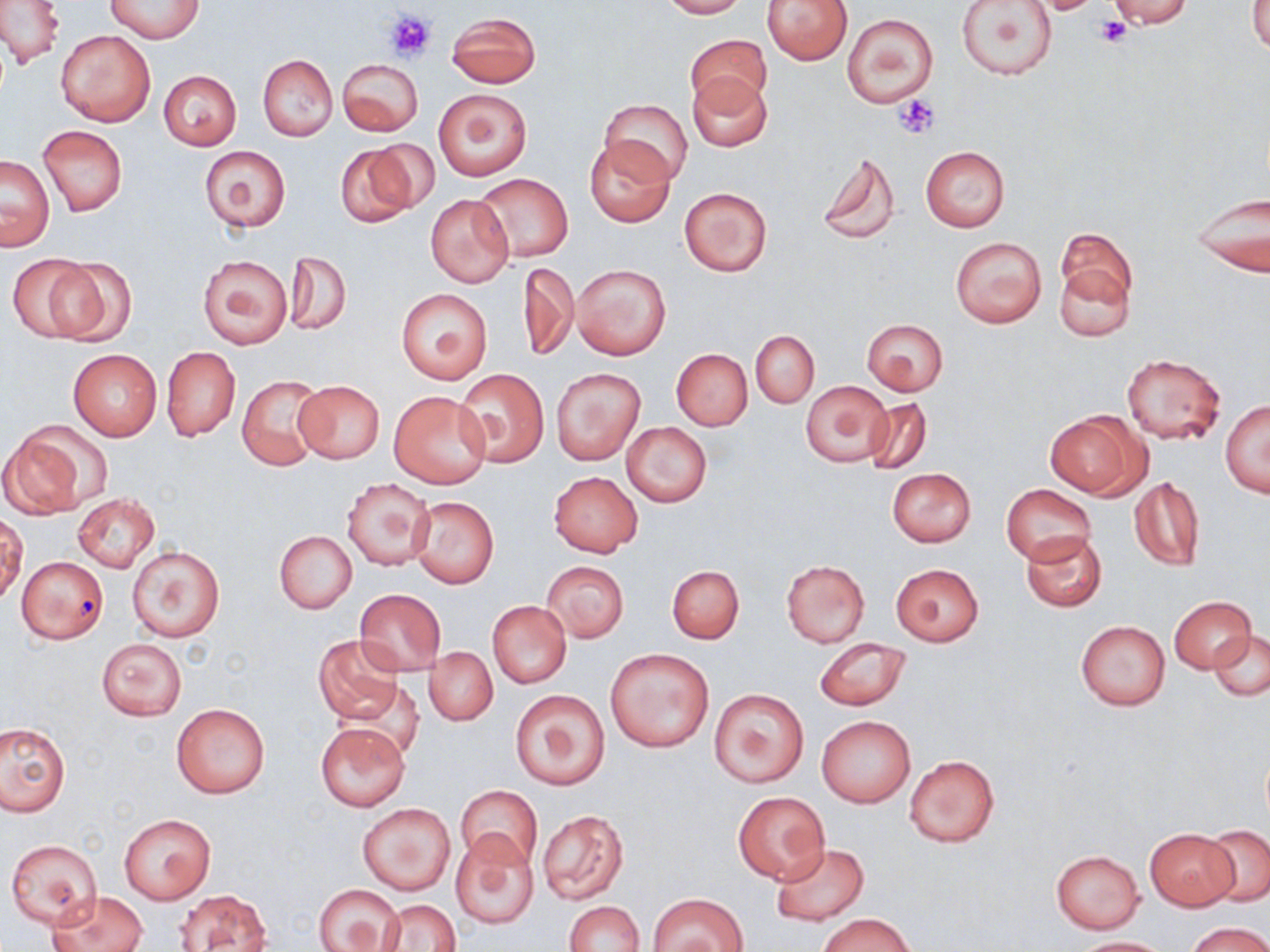
Summary:
  - Coordinate format: approximate bounding boxes as (x1,y1)-(x2,y2) corner pairs in pixels
  - Uninfected red blood cell locations: (0,0)-(64,68), (106,0)-(203,43), (658,0)-(746,18), (763,0)-(853,65), (956,0)-(1057,81), (1028,0)-(1109,15), (1106,0)-(1195,28), (1249,1)-(1270,54), (447,12)-(541,88), (843,14)-(937,107), (686,28)-(771,111), (55,29)-(155,126), (257,54)-(337,140), (338,58)-(423,136), (159,70)-(242,150), (687,72)-(772,151), (433,88)-(532,180), (599,99)-(693,186), (38,125)-(127,215), (584,138)-(676,226), (364,139)-(441,214), (335,143)-(422,229), (199,146)-(290,232), (920,146)-(1010,231), (816,149)-(901,245), (1,155)-(55,250), (473,173)-(573,262), (678,186)-(773,276), (1190,190)-(1269,279), (425,194)-(514,287), (1058,226)-(1139,314), (949,237)-(1047,327), (285,251)-(351,335), (6,253)-(101,341), (196,255)-(291,349), (47,257)-(137,347), (1054,258)-(1134,341), (518,261)-(577,360), (572,263)-(672,362), (398,288)-(492,384), (861,319)-(948,395), (751,331)-(818,408), (161,347)-(240,442), (68,349)-(161,441), (671,349)-(752,431), (1122,354)-(1225,445), (551,368)-(645,465), (454,370)-(550,467), (237,374)-(326,471), (294,379)-(384,463), (800,380)-(892,467), (389,391)-(493,489), (864,397)-(932,476), (1221,400)-(1270,496), (1046,409)-(1147,500), (621,423)-(711,508), (0,426)-(95,519), (887,468)-(976,547), (549,472)-(643,557), (341,476)-(436,570), (1129,477)-(1204,570), (1003,483)-(1095,565), (72,494)-(159,572), (410,495)-(499,587), (1,515)-(27,604), (1021,530)-(1106,611), (274,532)-(357,613), (127,544)-(227,642), (15,557)-(107,644), (781,560)-(869,647), (541,561)-(629,642), (891,563)-(983,645), (668,565)-(743,643), (353,589)-(447,676), (1168,596)-(1256,673), (486,600)-(571,688), (1075,621)-(1170,710), (1210,630)-(1269,701), (312,634)-(404,726), (814,638)-(912,712), (97,639)-(187,720), (424,648)-(497,726), (605,649)-(714,752), (709,688)-(809,787), (511,689)-(610,791), (171,703)-(271,799), (816,715)-(916,808), (1,721)-(70,815), (316,722)-(409,811), (904,755)-(999,848), (457,785)-(542,869), (733,792)-(829,883), (357,801)-(456,895), (537,809)-(629,904), (118,813)-(216,905), (1202,825)-(1270,906), (1145,828)-(1238,910), (451,830)-(539,930), (5,839)-(103,929), (770,843)-(870,927), (1050,849)-(1145,932), (314,883)-(404,952), (174,889)-(271,951), (48,890)-(147,952), (649,893)-(747,951), (376,900)-(461,951), (563,900)-(645,952), (820,913)-(913,952), (1186,922)-(1268,952), (1072,937)-(1170,951)
  - Platelet locations: (384,9)-(435,61), (1097,17)-(1132,47), (894,96)-(939,139)
  - Slide-level diagnosis: no evidence of blood parasites
  - Field of view: one of a larger specimen
  - Modality: optical microscopy
  - Image size: 1270×952 pixels
  - Preparation: thin blood smear
  - Magnification: 1000x
  - Stain: May-Grünwald-Giemsa